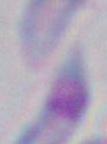

identification = Toxoplasma gondii
magnification = 1000x
modality = micrograph